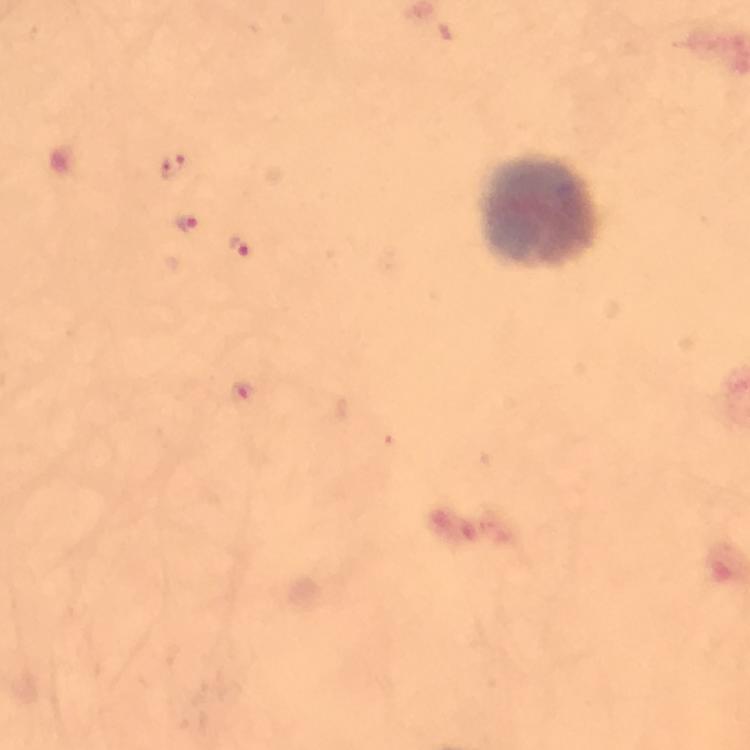
capture = smartphone camera through the microscope
magnification = 100x
context = from a diagnostic examination for malaria
image size = 750×750 pixels
malaria parasite locations = approximate object centers, in pixels from the top-left corner: (x=172, y=168), (x=188, y=225), (x=239, y=248), (x=241, y=394)
immersion oil = applied
leukocyte locations = approximate object centers, in pixels from the top-left corner: (x=540, y=214)
stain = Giemsa
cropped from = one field of view
preparation = thick blood smear